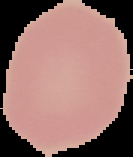
From a thin blood film. The area outside the segmented cell region is set to black. Image is 133×157 pixels. Result: negative for malaria parasites.